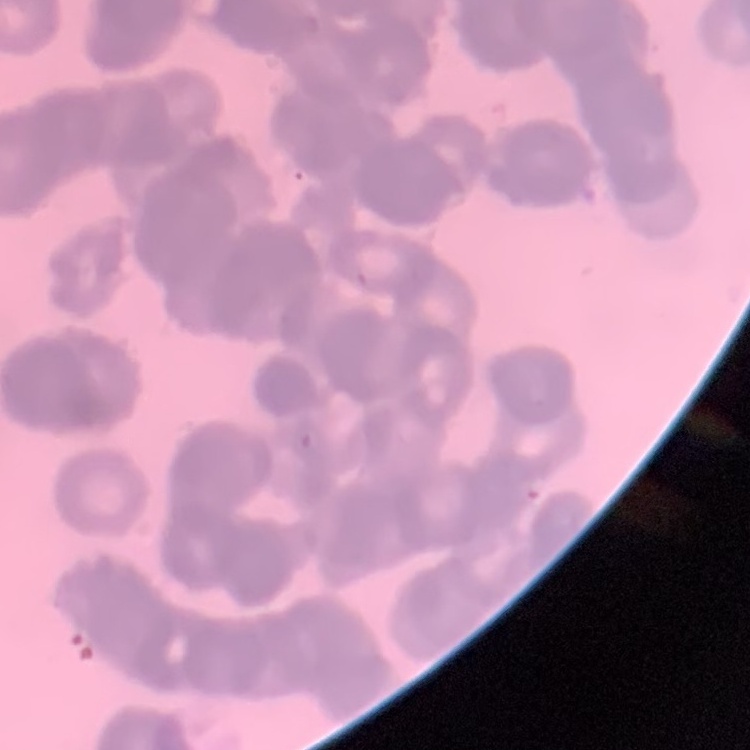

The red blood cells show rouleaux formation. Thin blood smear. Square crop of a larger photomicrograph. Field's or Giemsa stain.